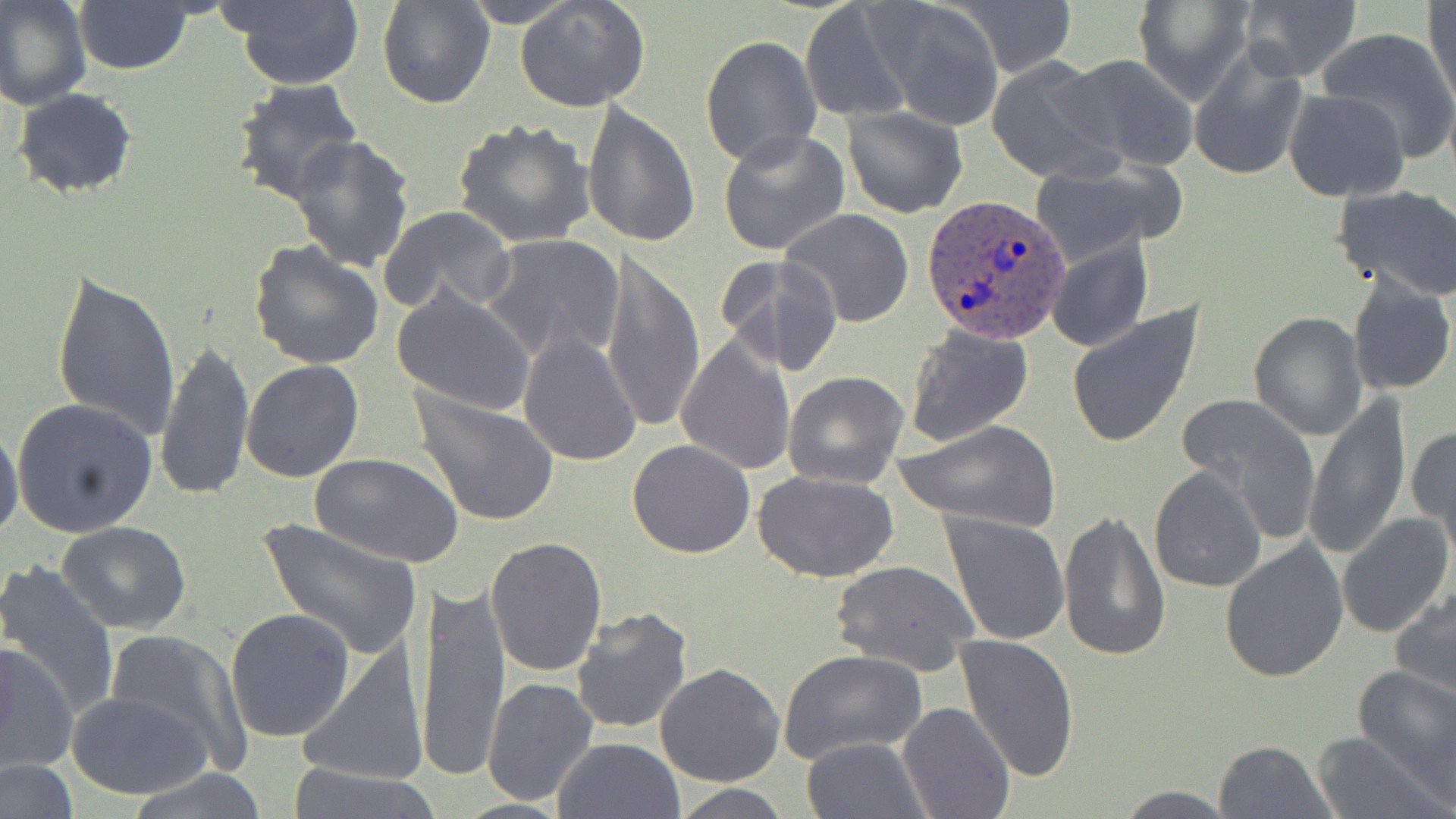
Summary:
  - Coordinate format: approximate bounding boxes as named x1/y1/x2/y2 corners in pixels
  - Uninfected red blood cell locations: (x1=0, y1=0, x2=91, y2=109), (x1=375, y1=0, x2=494, y2=109), (x1=460, y1=0, x2=580, y2=27), (x1=514, y1=0, x2=653, y2=114), (x1=954, y1=0, x2=1077, y2=77), (x1=1131, y1=0, x2=1253, y2=104), (x1=73, y1=1, x2=193, y2=75), (x1=227, y1=1, x2=364, y2=89), (x1=1237, y1=1, x2=1362, y2=81), (x1=1425, y1=1, x2=1455, y2=109), (x1=873, y1=2, x2=1005, y2=131), (x1=800, y1=3, x2=913, y2=121), (x1=1315, y1=26, x2=1456, y2=162), (x1=700, y1=33, x2=822, y2=169), (x1=1187, y1=41, x2=1308, y2=181), (x1=1061, y1=54, x2=1198, y2=172), (x1=988, y1=57, x2=1119, y2=182), (x1=231, y1=79, x2=366, y2=205), (x1=13, y1=88, x2=139, y2=199), (x1=1283, y1=89, x2=1410, y2=203), (x1=584, y1=100, x2=703, y2=251), (x1=842, y1=106, x2=967, y2=218), (x1=453, y1=120, x2=595, y2=248), (x1=719, y1=128, x2=849, y2=255), (x1=288, y1=136, x2=415, y2=272), (x1=1024, y1=167, x2=1170, y2=267), (x1=1331, y1=183, x2=1456, y2=302), (x1=378, y1=205, x2=516, y2=316), (x1=781, y1=209, x2=914, y2=328), (x1=1044, y1=232, x2=1152, y2=353), (x1=480, y1=234, x2=626, y2=365), (x1=246, y1=239, x2=385, y2=371), (x1=719, y1=253, x2=845, y2=377), (x1=600, y1=254, x2=707, y2=435), (x1=50, y1=270, x2=182, y2=441), (x1=1347, y1=273, x2=1455, y2=396), (x1=392, y1=286, x2=536, y2=417), (x1=1065, y1=303, x2=1205, y2=449), (x1=1248, y1=312, x2=1368, y2=440), (x1=904, y1=326, x2=1034, y2=448), (x1=517, y1=330, x2=642, y2=467), (x1=676, y1=332, x2=797, y2=475), (x1=155, y1=337, x2=253, y2=501), (x1=241, y1=359, x2=364, y2=483), (x1=784, y1=371, x2=909, y2=489), (x1=410, y1=386, x2=559, y2=528), (x1=1174, y1=394, x2=1320, y2=539), (x1=1303, y1=394, x2=1411, y2=559), (x1=12, y1=397, x2=158, y2=538), (x1=893, y1=419, x2=1060, y2=531), (x1=0, y1=420, x2=24, y2=545), (x1=1408, y1=425, x2=1456, y2=545), (x1=627, y1=438, x2=756, y2=559), (x1=312, y1=455, x2=461, y2=568), (x1=1149, y1=465, x2=1267, y2=595), (x1=754, y1=470, x2=899, y2=582), (x1=1058, y1=509, x2=1171, y2=662), (x1=940, y1=511, x2=1072, y2=646), (x1=1336, y1=513, x2=1453, y2=640), (x1=257, y1=518, x2=422, y2=660), (x1=57, y1=521, x2=191, y2=635), (x1=485, y1=535, x2=608, y2=679), (x1=1220, y1=540, x2=1348, y2=685), (x1=831, y1=560, x2=978, y2=676), (x1=0, y1=562, x2=120, y2=720), (x1=415, y1=579, x2=509, y2=780), (x1=1391, y1=585, x2=1456, y2=702), (x1=570, y1=606, x2=692, y2=735), (x1=224, y1=607, x2=356, y2=742), (x1=104, y1=629, x2=251, y2=771), (x1=954, y1=634, x2=1079, y2=784), (x1=0, y1=640, x2=80, y2=777), (x1=295, y1=648, x2=427, y2=787), (x1=778, y1=648, x2=926, y2=765), (x1=655, y1=663, x2=785, y2=786), (x1=1353, y1=664, x2=1456, y2=796), (x1=482, y1=678, x2=598, y2=807), (x1=67, y1=690, x2=215, y2=800), (x1=899, y1=701, x2=1014, y2=819), (x1=1310, y1=732, x2=1438, y2=818), (x1=801, y1=736, x2=928, y2=819), (x1=553, y1=737, x2=686, y2=819), (x1=1211, y1=739, x2=1338, y2=819), (x1=0, y1=756, x2=80, y2=818), (x1=281, y1=762, x2=445, y2=819), (x1=126, y1=767, x2=274, y2=818), (x1=671, y1=782, x2=790, y2=817), (x1=1112, y1=785, x2=1239, y2=817)
  - Plasmodium ovale-infected red blood cell locations: (x1=921, y1=195, x2=1071, y2=344)
  - Slide-level diagnosis: Plasmodium ovale
  - Field of view: single
  - Modality: light microscopy
  - Image size: 1456×819 pixels
  - Preparation: thin blood smear
  - Stain: May-Grünwald-Giemsa
  - Magnification: 1000x